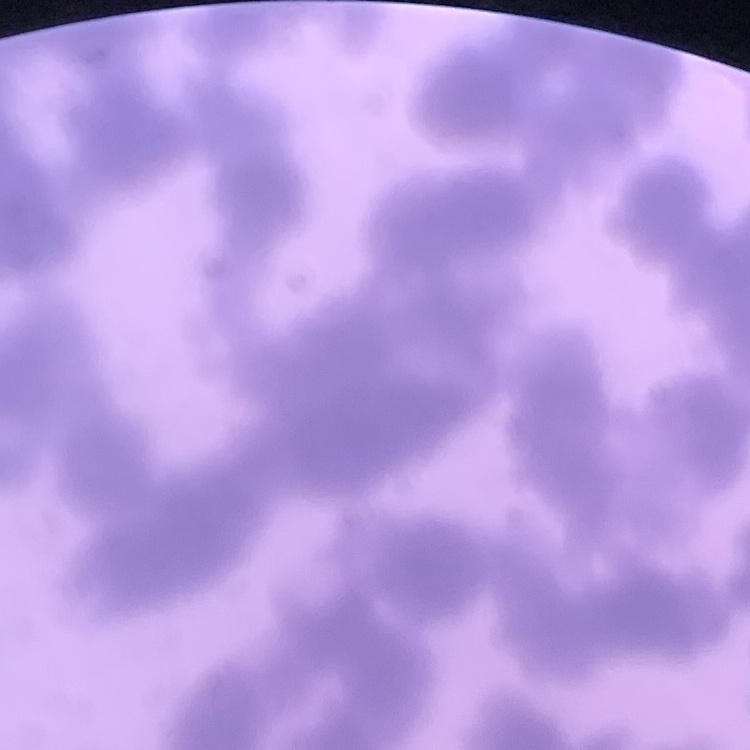
The red blood cells show rouleaux formation. Field's or Giemsa stain. Square crop of a larger photomicrograph. Thin blood film.